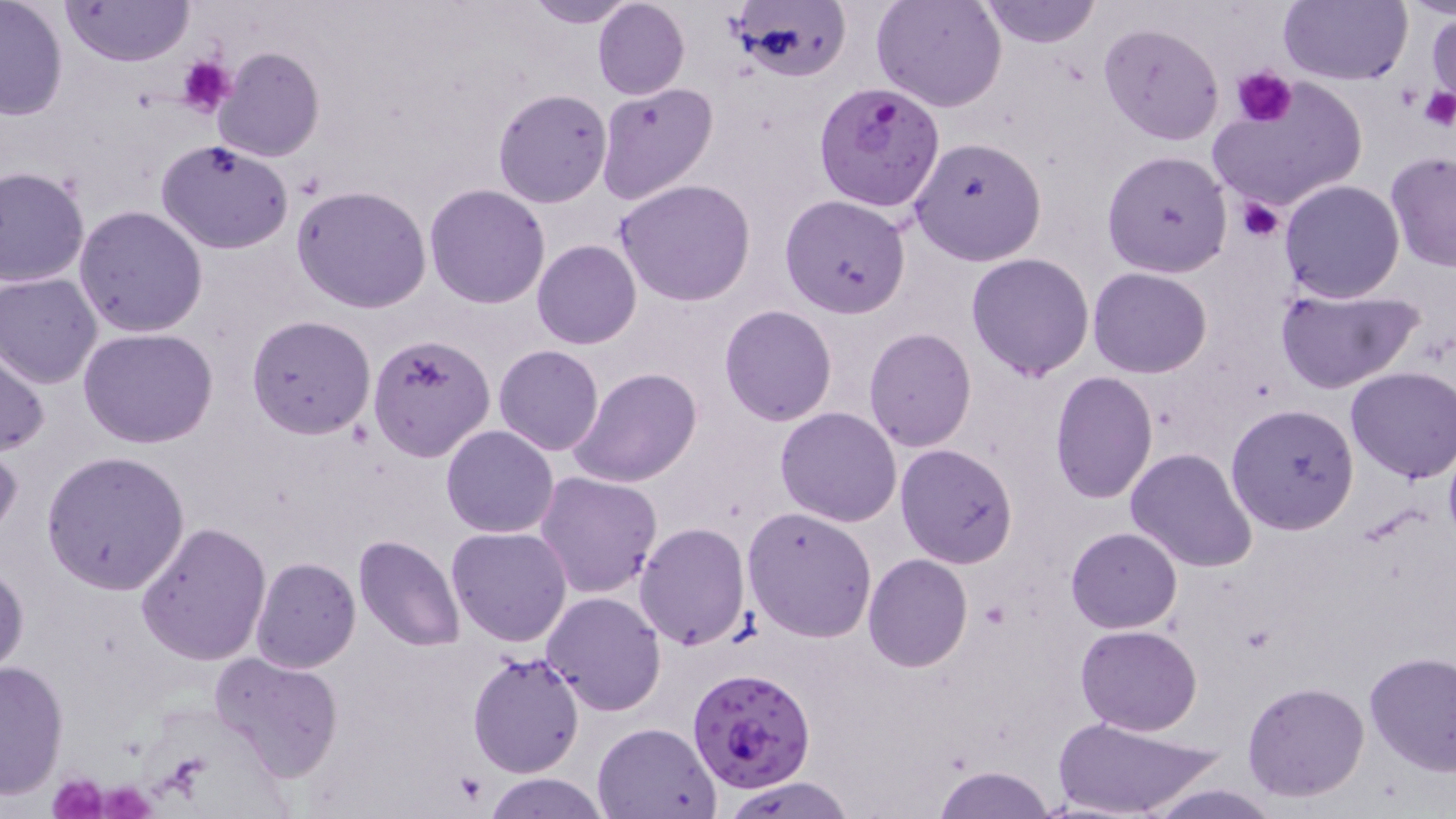
{
  "slide_level_diagnosis": "Plasmodium falciparum",
  "modality": "light microscopy",
  "stain": "May-Grünwald-Giemsa",
  "preparation": "thin blood film",
  "plasmodium_falciparum_infected_red_blood_cell_locations": "approximate bounding boxes as (x1, y1, x2, y2) in pixels: (813, 81, 945, 214), (687, 667, 817, 793)",
  "platelet_locations": "approximate bounding boxes as (x1, y1, x2, y2) in pixels: (178, 54, 234, 119), (1231, 67, 1297, 128), (1419, 86, 1454, 129), (1238, 198, 1287, 242), (453, 772, 483, 805), (46, 774, 109, 818), (105, 780, 155, 818)",
  "uninfected_red_blood_cell_locations": "approximate bounding boxes as (x1, y1, x2, y2) in pixels: (0, 0, 69, 122), (517, 0, 640, 27), (592, 0, 689, 100), (726, 0, 851, 82), (872, 0, 1008, 113), (978, 0, 1099, 47), (1278, 0, 1410, 86), (62, 1, 195, 66), (1427, 10, 1455, 110), (1098, 22, 1225, 146), (212, 46, 325, 163), (1208, 77, 1367, 214), (596, 82, 719, 205), (492, 88, 612, 207), (910, 136, 1048, 265), (157, 139, 296, 254), (1103, 150, 1232, 277), (1384, 153, 1456, 272), (0, 165, 90, 289), (615, 178, 756, 305), (1278, 180, 1405, 302), (424, 184, 551, 308), (292, 185, 433, 315), (779, 194, 912, 317), (73, 205, 208, 338), (532, 240, 641, 350), (0, 246, 171, 375), (967, 253, 1094, 380), (1088, 267, 1213, 379), (0, 273, 102, 388), (1275, 286, 1423, 394), (720, 305, 836, 426), (247, 315, 377, 439), (863, 327, 976, 451), (79, 328, 221, 449), (367, 329, 496, 464), (1, 343, 49, 457), (493, 345, 604, 457), (571, 367, 702, 488), (1344, 367, 1456, 483), (1050, 372, 1158, 504), (1227, 403, 1359, 536), (775, 407, 902, 527), (441, 425, 559, 538), (0, 439, 21, 545), (894, 443, 1018, 567), (1125, 447, 1258, 573), (42, 452, 191, 595), (535, 472, 662, 599), (743, 507, 877, 642), (135, 521, 272, 666), (634, 521, 751, 651), (1066, 526, 1181, 634), (445, 527, 573, 647), (354, 534, 467, 653), (863, 555, 972, 672), (250, 557, 361, 672), (1, 559, 28, 677), (542, 591, 668, 715), (1074, 623, 1203, 734), (211, 651, 343, 783), (1362, 651, 1456, 774), (468, 652, 584, 779), (0, 658, 69, 799), (1242, 680, 1371, 802), (1049, 714, 1229, 819), (593, 721, 720, 818), (932, 764, 1057, 818), (484, 774, 611, 818), (722, 777, 855, 818), (1139, 783, 1284, 817)",
  "field_of_view": "single",
  "magnification": "1000x",
  "image_size": "1456×819 pixels"
}